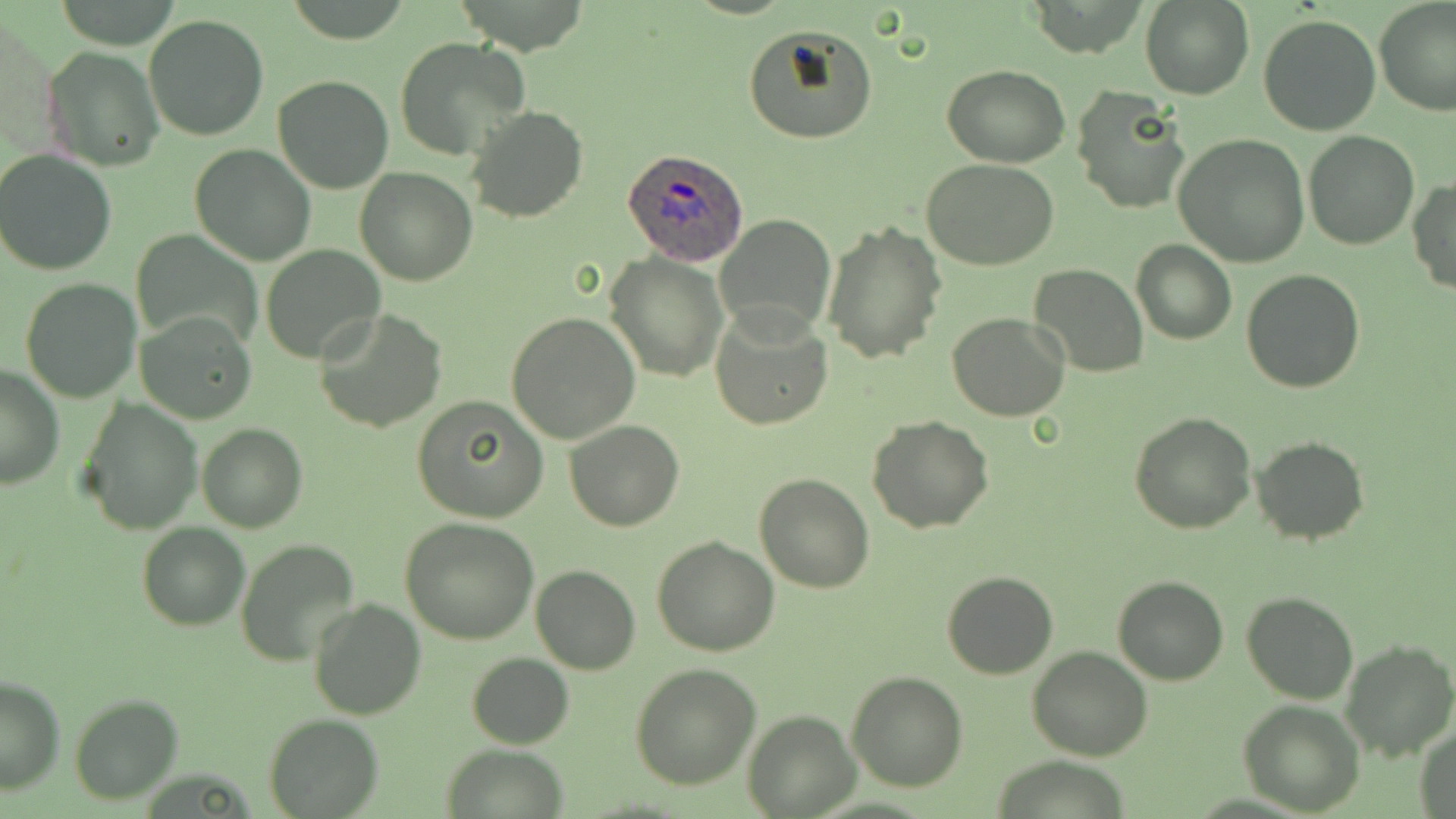

Summary:
  - Coordinate format: approximate bounding boxes as (x1, y1, x2, y2) in pixels
  - Plasmodium ovale-infected red blood cell locations: (623, 146, 749, 267)
  - Uninfected red blood cell locations: (1373, 0, 1456, 117), (1140, 1, 1253, 99), (144, 14, 268, 141), (1258, 14, 1380, 134), (742, 24, 877, 145), (393, 38, 530, 162), (41, 46, 164, 170), (941, 64, 1069, 166), (273, 75, 395, 193), (1071, 86, 1190, 216), (464, 104, 587, 223), (1304, 131, 1418, 249), (1174, 134, 1311, 266), (188, 145, 315, 266), (0, 149, 118, 277), (922, 159, 1062, 272), (355, 168, 476, 286), (1408, 179, 1456, 296), (714, 214, 838, 340), (822, 220, 945, 363), (136, 232, 259, 348), (1131, 239, 1238, 345), (260, 245, 386, 363), (603, 252, 728, 381), (1027, 264, 1149, 379), (1242, 269, 1365, 394), (21, 278, 141, 402), (709, 305, 834, 431), (138, 308, 255, 423), (315, 310, 447, 433), (947, 311, 1071, 422), (506, 313, 641, 444), (1, 365, 64, 489), (411, 396, 549, 522), (78, 399, 203, 535), (1128, 411, 1258, 534), (867, 416, 995, 533), (564, 419, 684, 531), (196, 422, 307, 533), (1251, 436, 1368, 544), (754, 472, 875, 593), (400, 519, 540, 645), (137, 523, 250, 630), (651, 536, 779, 658), (235, 539, 361, 665), (532, 565, 640, 674), (940, 570, 1059, 678), (1113, 576, 1228, 685), (1242, 591, 1359, 705), (308, 598, 427, 719), (1341, 640, 1456, 762), (1026, 646, 1153, 762), (466, 652, 574, 748), (631, 664, 759, 788), (845, 671, 967, 792), (0, 676, 65, 794), (68, 693, 182, 805), (1237, 701, 1365, 816), (743, 710, 858, 817), (263, 714, 384, 819), (1414, 724, 1456, 818), (440, 745, 569, 818)
  - Slide-level diagnosis: Plasmodium ovale
  - Field of view: one of a larger specimen
  - Image size: 1456×819 pixels
  - Preparation: thin blood film
  - Stain: May-Grünwald-Giemsa
  - Magnification: 1000x
  - Modality: light microscopy